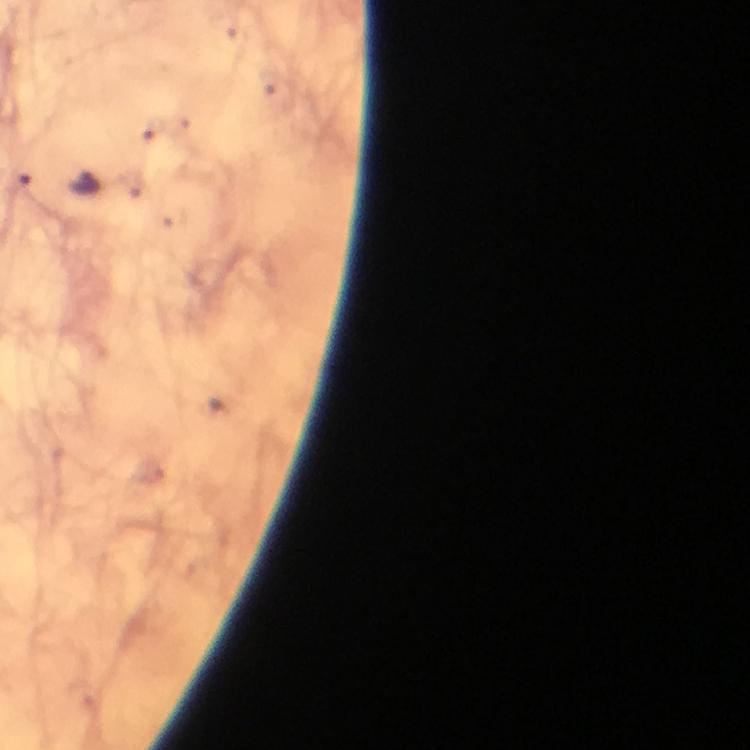

Approximate centers as {x, y} in pixels.
Summary:
  - Malaria parasite locations: {85, 186}
  - Magnification: 100x
  - Image size: 750×750 pixels
  - Capture: smartphone mounted on the microscope
  - Immersion oil: applied
  - Stain: Giemsa
  - Preparation: thick blood film
  - Context: from a diagnostic examination for malaria
  - Cropped from: a single field of view